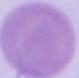

modality = photomicrograph
magnification = 1000x
identification = erythrocyte